Classify this cell by malaria status.
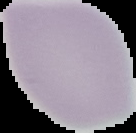
It is uninfected.

image type = segmented cell region on a black background
preparation = thin blood smear
image size = 136×133 pixels